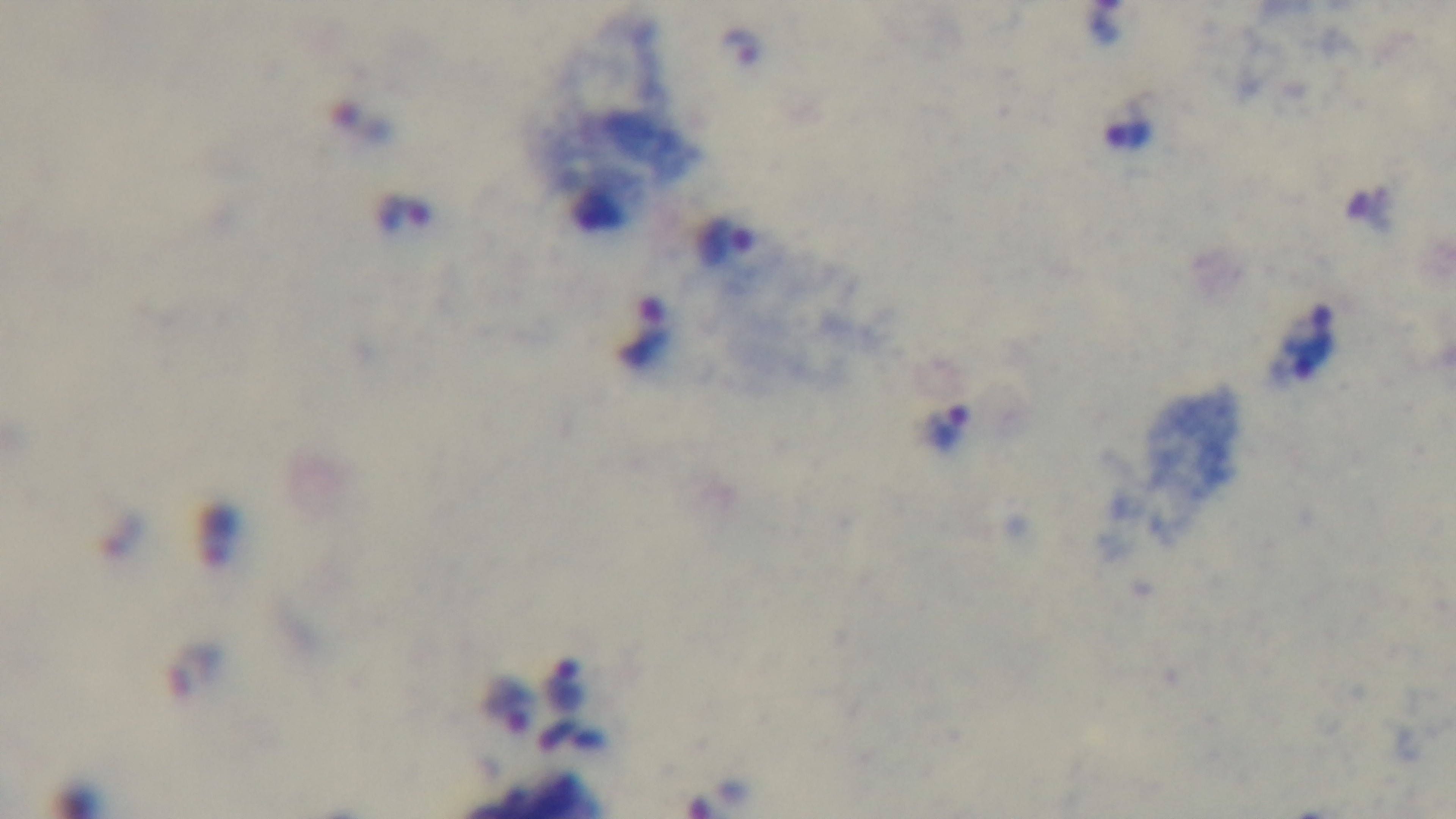 One field from the slide. Preparation: thick smear. Giemsa stain. Malaria status: infected. Oil-immersion objective, 100x. Mounted 4K digital camera. Light microscopy.